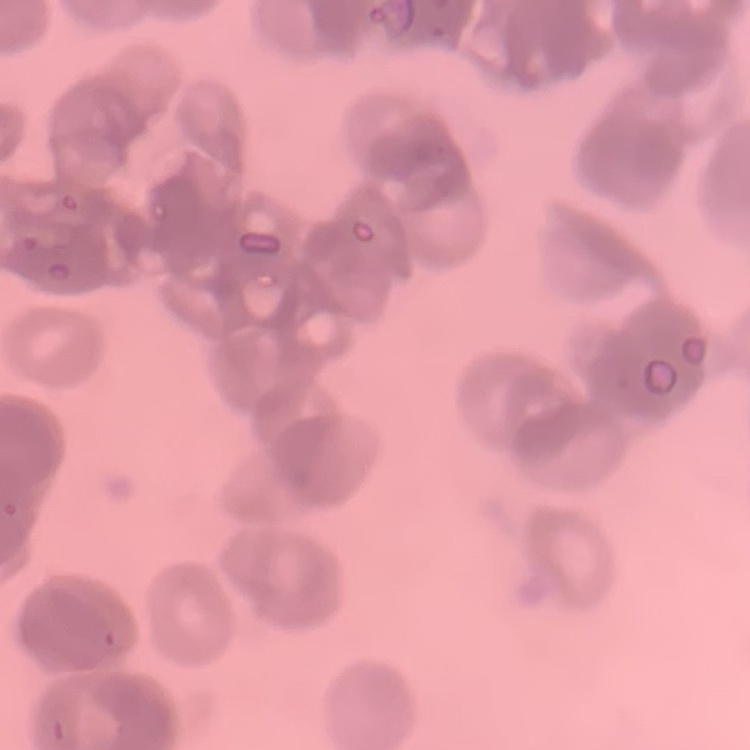

The erythrocytes exhibit rouleaux formation. Stained with either Field's or Giemsa. Thin peripheral smear. Square crop of a larger photomicrograph.